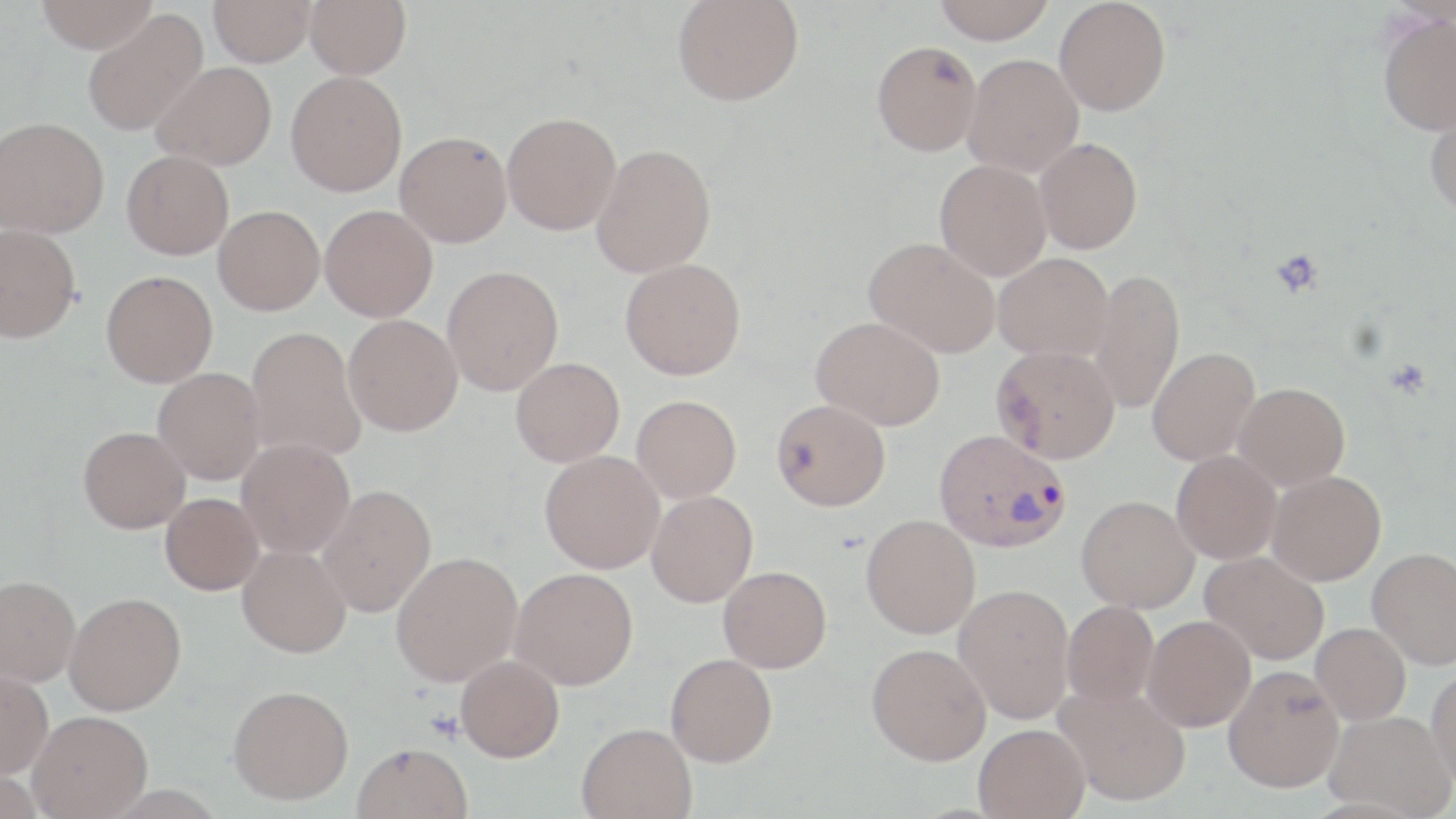

slide_level_diagnosis: Plasmodium vivax
preparation: thin blood smear
modality: optical microscopy
stain: May-Grünwald-Giemsa
image_size: 1456×819 pixels
platelet_locations: 'approximate bounding boxes as (x1,y1)-(x2,y2) corner pairs in pixels: (1270,248)-(1325,298)'
uninfected_red_blood_cell_locations: 'approximate bounding boxes as (x1,y1)-(x2,y2) corner pairs in pixels: (34,0)-(158,53), (209,0)-(317,66), (305,0)-(411,79), (933,0)-(1055,43), (1054,0)-(1171,116), (672,1)-(804,106), (82,9)-(208,136), (1377,11)-(1456,135), (871,40)-(981,156), (962,54)-(1084,177), (151,61)-(277,170), (286,71)-(407,196), (1424,101)-(1456,219), (502,112)-(621,235), (0,117)-(109,238), (395,131)-(512,247), (1035,137)-(1142,254), (592,143)-(716,278), (122,150)-(234,259), (935,159)-(1052,280), (213,205)-(324,315), (320,205)-(437,322), (0,224)-(81,342), (864,237)-(1000,359), (993,253)-(1114,361), (620,258)-(746,380), (442,266)-(563,396), (1088,268)-(1185,415), (101,270)-(217,387), (343,314)-(463,436), (811,316)-(945,430), (245,326)-(367,462), (991,344)-(1120,463), (1147,346)-(1260,465), (511,357)-(624,466), (153,367)-(265,484), (1234,382)-(1350,491), (632,394)-(741,502), (771,398)-(890,511), (78,426)-(190,533), (236,438)-(355,558), (539,450)-(664,573), (1171,450)-(1281,564), (1267,470)-(1386,585), (316,485)-(436,617), (646,490)-(757,607), (160,493)-(264,595), (1077,495)-(1199,612), (861,514)-(981,639), (237,544)-(351,658), (1367,547)-(1456,669), (391,551)-(522,686), (1200,551)-(1329,665), (718,565)-(832,672), (509,567)-(638,690), (0,574)-(80,687), (953,583)-(1075,724), (64,592)-(186,715), (1062,600)-(1159,709), (1142,615)-(1255,732), (1310,622)-(1411,726), (866,643)-(991,765), (665,653)-(777,767), (456,655)-(564,762), (1223,664)-(1345,793), (1427,667)-(1456,793), (0,668)-(53,778), (1055,683)-(1191,807), (227,684)-(354,805), (28,710)-(153,818), (1324,710)-(1454,817), (577,722)-(697,819), (974,723)-(1089,818), (352,742)-(472,819)'
field_of_view: one of a larger specimen
plasmodium_vivax_infected_red_blood_cell_locations: 'approximate bounding boxes as (x1,y1)-(x2,y2) corner pairs in pixels: (934,429)-(1071,553)'
magnification: 1000x